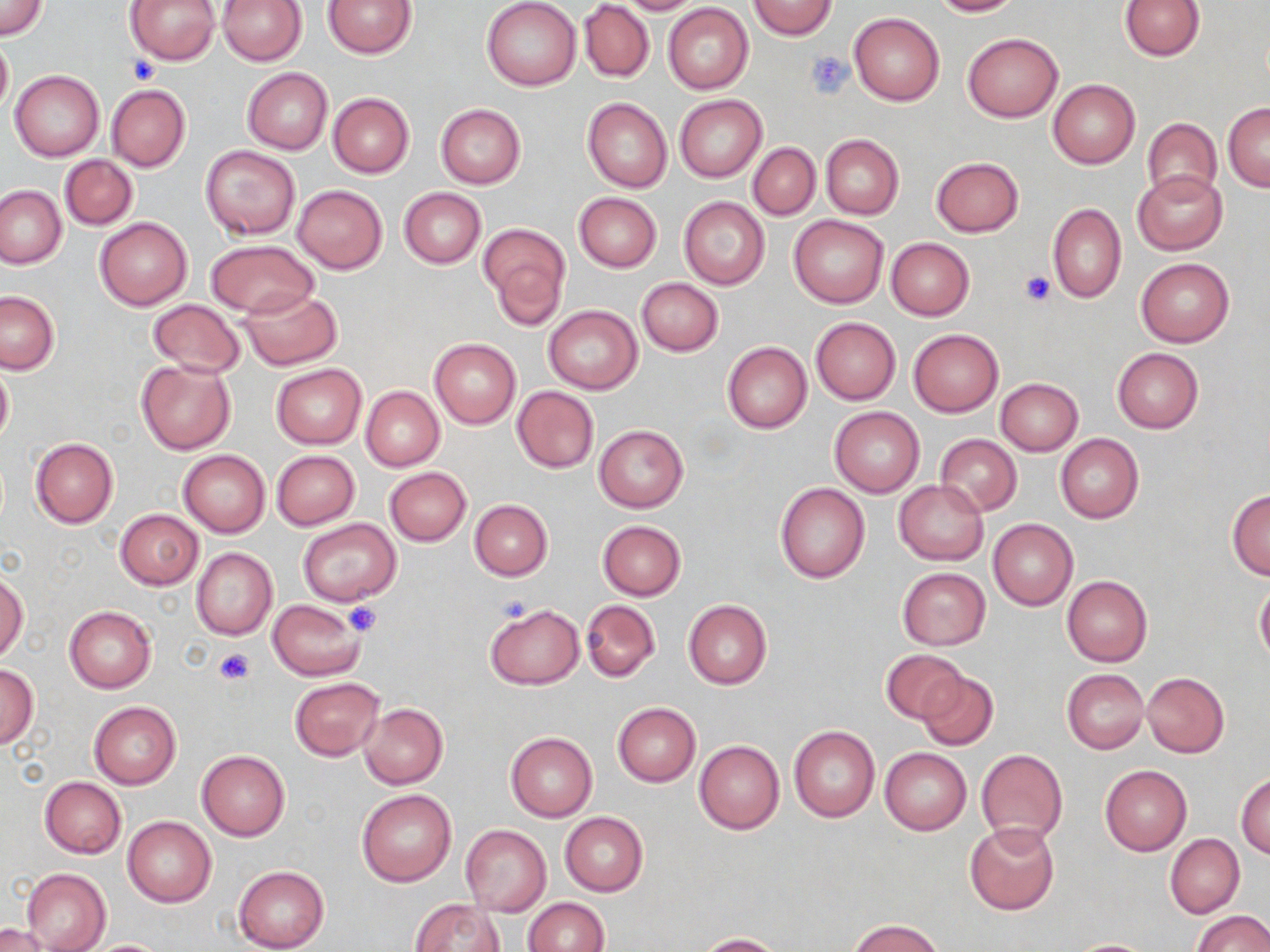
Approximate bounding boxes as (x1,y1)-(x2,y2) corner pairs in pixels. Platelet locations: (805,52)-(853,99), (126,56)-(160,84), (1018,270)-(1055,306), (492,592)-(535,627), (344,601)-(383,637), (214,648)-(253,686). Uninfected red blood cell locations: (126,0)-(220,64), (216,0)-(307,65), (324,0)-(417,58), (481,0)-(581,91), (616,0)-(706,14), (929,0)-(1022,16), (0,1)-(48,41), (747,1)-(838,39), (1120,1)-(1206,61), (580,2)-(653,82), (663,4)-(753,94), (849,12)-(945,105), (963,32)-(1062,121), (0,34)-(12,121), (242,68)-(333,154), (10,70)-(105,160), (1047,80)-(1140,168), (106,84)-(191,171), (327,92)-(414,177), (674,94)-(768,183), (582,97)-(673,193), (1223,102)-(1270,191), (435,104)-(526,189), (1140,117)-(1222,204), (821,134)-(903,219), (748,142)-(820,220), (200,145)-(300,239), (60,155)-(137,229), (931,156)-(1025,236), (1133,170)-(1227,255), (0,184)-(65,268), (292,185)-(387,274), (399,187)-(486,268), (573,194)-(661,273), (678,197)-(770,289), (1047,204)-(1126,303), (788,214)-(889,308), (94,217)-(192,310), (479,222)-(569,326), (885,238)-(973,320), (204,239)-(318,319), (1135,258)-(1235,348), (636,278)-(723,355), (238,288)-(343,370), (0,291)-(59,375), (148,299)-(245,378), (543,306)-(641,394), (811,317)-(900,405), (908,329)-(1004,417), (428,338)-(520,429), (722,341)-(812,433), (1112,348)-(1203,434), (135,359)-(236,454), (0,361)-(13,448), (271,364)-(365,449), (995,377)-(1083,455), (512,386)-(599,473), (360,387)-(444,472), (830,406)-(924,498), (593,424)-(688,513), (1056,433)-(1144,524), (935,434)-(1022,516), (29,437)-(118,528), (179,450)-(270,537), (272,451)-(359,530), (384,467)-(471,545), (893,480)-(987,565), (774,482)-(868,583), (1226,489)-(1270,580), (470,499)-(552,580), (115,509)-(203,589), (298,519)-(401,606), (989,519)-(1078,610), (596,520)-(686,600), (191,547)-(277,640), (897,568)-(991,650), (0,570)-(28,661), (1062,575)-(1153,667), (1254,582)-(1270,665), (268,599)-(366,680), (580,599)-(660,681), (683,600)-(772,690), (484,603)-(583,689), (64,605)-(157,693), (880,649)-(967,726), (1,664)-(38,748), (916,669)-(998,753), (1062,669)-(1148,753), (1142,672)-(1230,759), (290,678)-(384,761), (88,702)-(181,790), (611,702)-(700,787), (358,703)-(447,789), (789,726)-(880,822), (505,732)-(598,822), (695,740)-(784,834), (879,747)-(971,834), (975,749)-(1067,845), (196,750)-(289,840), (1099,765)-(1191,855), (1235,773)-(1270,858), (40,777)-(125,858), (357,788)-(457,887), (560,812)-(648,896), (122,816)-(216,907), (965,822)-(1059,915), (460,824)-(551,915), (1165,834)-(1244,917), (234,866)-(329,952), (20,868)-(110,952), (523,898)-(609,952), (408,899)-(503,952), (1193,911)-(1270,952), (846,918)-(947,952), (0,924)-(56,952), (696,932)-(783,951), (81,938)-(174,951), (1064,938)-(1159,951). Slide-level diagnosis: negative for blood parasites. Single field of view. May-Grünwald-Giemsa stain. Captured at 1000x magnification. Optical microscopy. Image is 1270×952 pixels. Thin blood film.